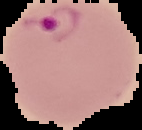 From a thin blood film. Result: malaria parasites detected. The area outside the segmented cell region is set to black. Image is 142×130 pixels.